Name the parasite shown.
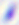

This is Toxoplasma gondii.

magnification = 400x
modality = micrograph